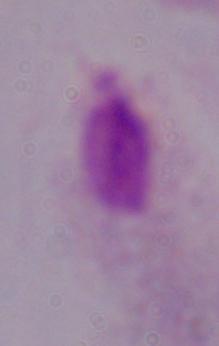

Summary:
  - Identification: trichomonad
  - Modality: micrograph
  - Magnification: 1000x